Assess this cell for malaria.
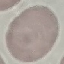

It is uninfected.

{
  "stain": "Giemsa",
  "image_type": "cell patch, automatically extracted from a larger field of view and resized to 64 × 64 pixels",
  "capture": "smartphone through the microscope eyepiece",
  "preparation": "thin blood smear"
}